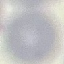
malaria_status: uninfected
capture: smartphone through the microscope eyepiece
stain: Giemsa
preparation: thin blood smear
image_type: cell patch, automatically extracted from a larger field of view and resized to 64 × 64 pixels